Classify this cell by malaria status.
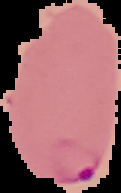

It is parasitized.

image type = cell region segmented out of the field of view; surrounding area masked to black
preparation = thin blood smear
image size = 121×193 pixels